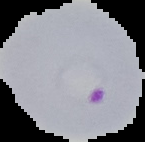
preparation = thin blood film
image size = 145×142 pixels
image type = segmented cell region on a black background
result = Plasmodium parasites identified